Classify this cell by malaria status.
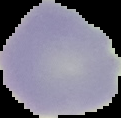

It is uninfected.

From a thin blood film. Image is 121×118 pixels. Cell region segmented out of the field of view; the surrounding area is masked to black.